Assess this cell for malaria.
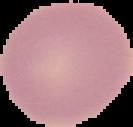

Uninfected.

From a thin blood smear. Image is 133×127 pixels. Cell region segmented out of the field of view; the surrounding area is masked to black.